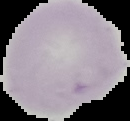

Image is 130×121 pixels. From a thin blood smear. Result: negative for malaria parasites. The area outside the segmented cell region is set to black.